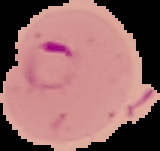
Summary:
  - Image type: cell region segmented out of the field of view; surrounding area masked to black
  - Result: malaria parasites detected
  - Preparation: thin blood film
  - Image size: 160×151 pixels